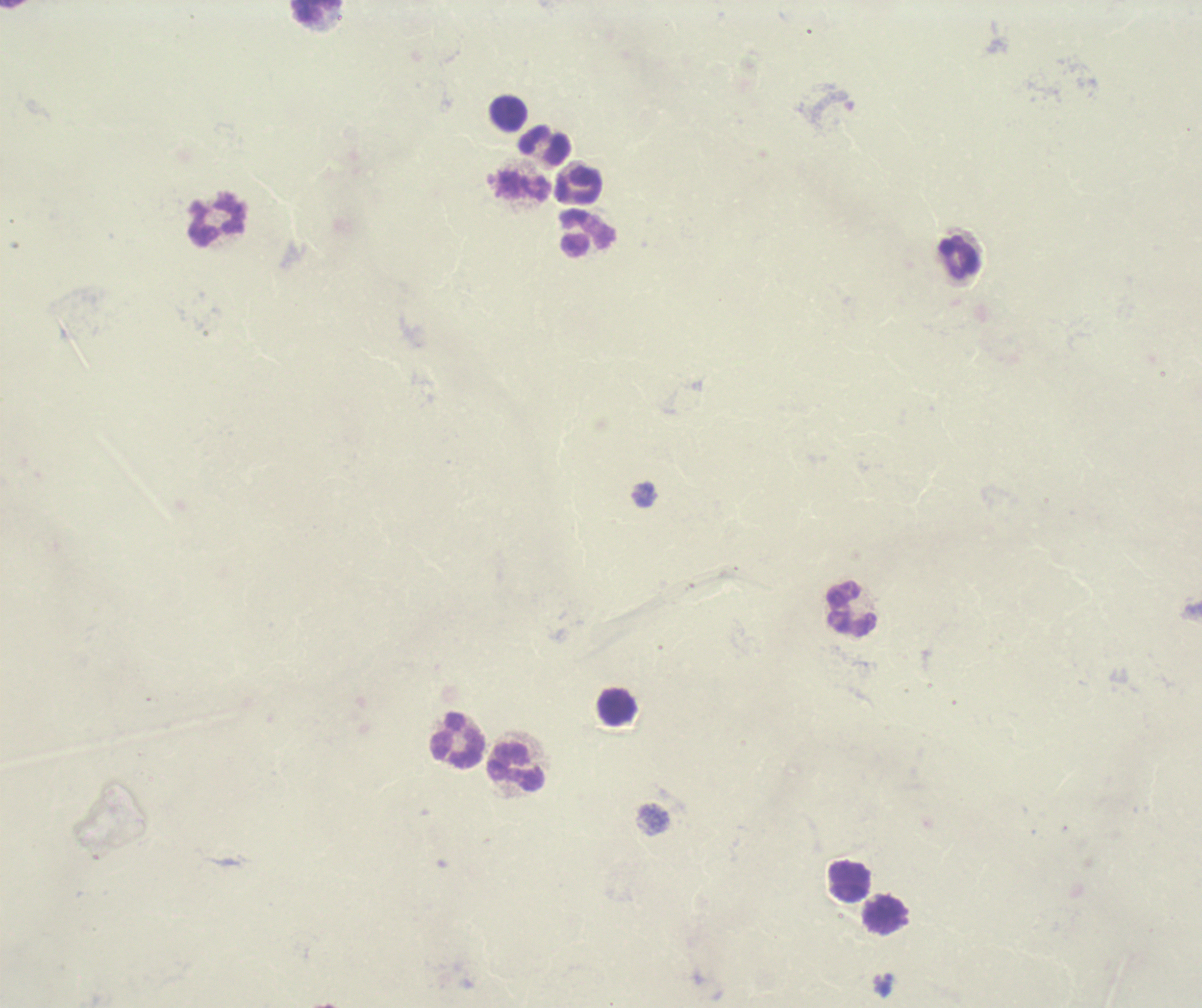
Approximate object centers, in pixels from the top-left corner. Leukocyte locations: (x=315, y=10), (x=509, y=115), (x=545, y=146), (x=578, y=185), (x=218, y=221), (x=587, y=233), (x=960, y=258), (x=853, y=611), (x=618, y=708), (x=458, y=740), (x=517, y=768), (x=850, y=881), (x=884, y=914). Romanowsky stain. Thick smear of blood. Result: no Plasmodium parasites detected. Background quality: poor. Image is 1202×1008 pixels. One field from this slide. Previously used in an actual diagnosis. 100x magnification.